Assess this cell for malaria.
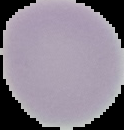

Uninfected.

From a thin blood smear. Segmented cell region on a black background. Image is 124×130 pixels.